Classify this cell by malaria status.
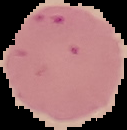
It is uninfected.

{
  "preparation": "thin blood film",
  "image_type": "cell region segmented out of the field of view; surrounding area masked to black",
  "image_size": "127×130 pixels"
}